Locate and identify every blood parasite.
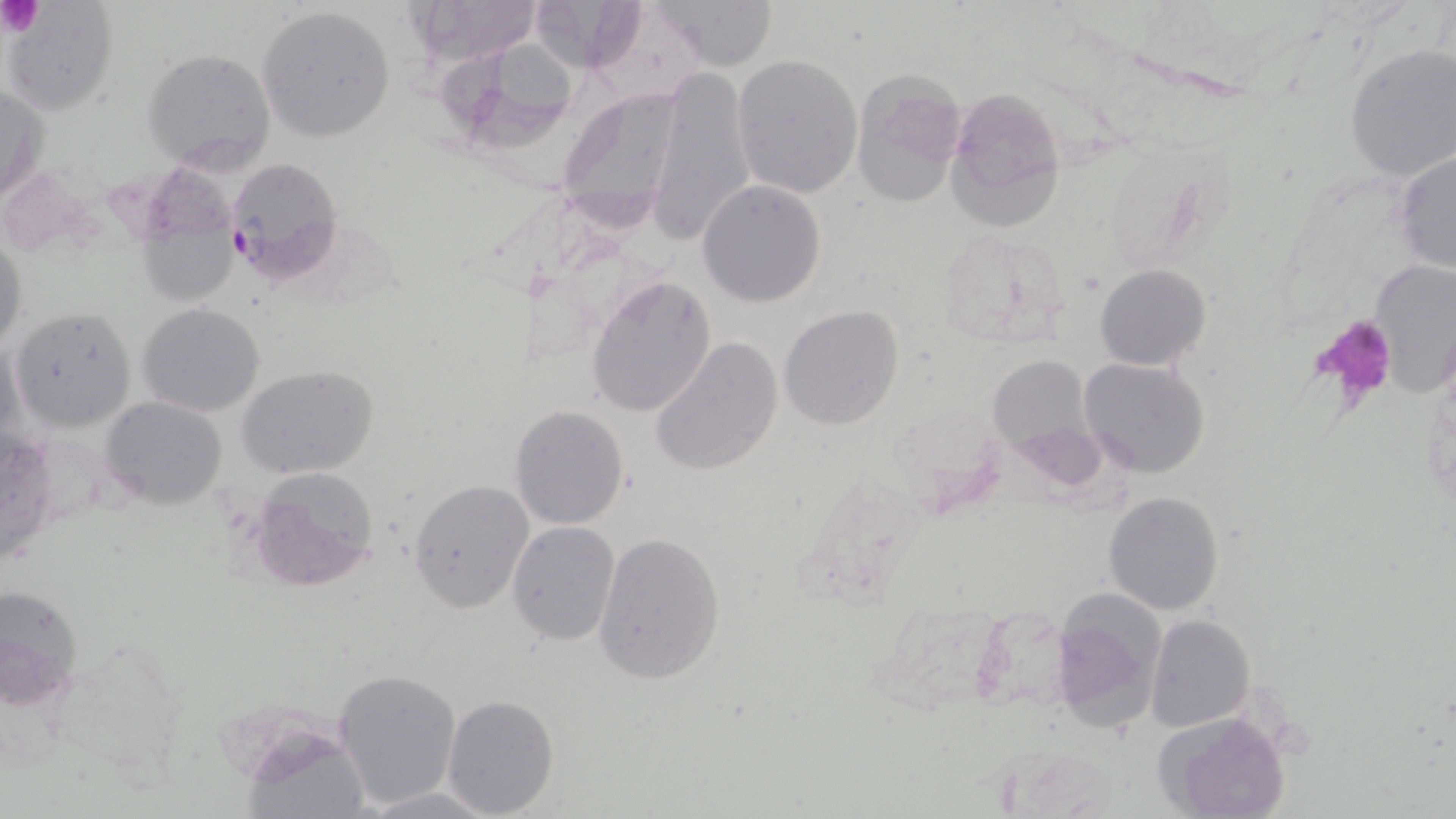

Approximate bounding boxes as (x1, y1, x2, y2) in pixels.
Plasmodium falciparum-infected red blood cells: (223, 157, 341, 280).
No Plasmodium ovale, Plasmodium malariae, Plasmodium vivax, Babesia divergens, or Trypanosoma brucei observed.

Summary:
  - Uninfected red blood cell locations: (408, 0, 547, 65), (532, 0, 650, 82), (650, 0, 779, 70), (4, 2, 118, 114), (258, 7, 398, 144), (1343, 45, 1456, 181), (437, 48, 579, 150), (142, 49, 275, 170), (732, 54, 862, 199), (645, 68, 756, 246), (849, 70, 966, 209), (1, 82, 48, 206), (556, 86, 692, 232), (943, 89, 1066, 231), (133, 151, 252, 304), (1393, 151, 1456, 276), (697, 180, 827, 307), (932, 229, 1070, 346), (0, 232, 27, 355), (1369, 258, 1456, 395), (1095, 263, 1210, 370), (585, 274, 717, 418), (137, 303, 264, 417), (778, 305, 905, 432), (11, 308, 137, 432), (649, 338, 783, 477), (988, 353, 1093, 457), (1079, 358, 1210, 479), (239, 364, 378, 480), (102, 395, 225, 509), (509, 405, 630, 530), (246, 468, 382, 594), (407, 478, 534, 616), (1103, 490, 1225, 616), (506, 521, 621, 646), (592, 529, 728, 686), (0, 583, 85, 709), (1048, 590, 1167, 735), (1146, 614, 1254, 732), (332, 668, 462, 808), (442, 694, 560, 817), (1160, 710, 1292, 819), (247, 731, 375, 818), (986, 742, 1128, 815), (361, 786, 497, 818)
  - Platelet locations: (0, 0, 45, 36), (1310, 315, 1398, 405)
  - Slide-level diagnosis: Plasmodium falciparum
  - Image size: 1456×819 pixels
  - Stain: May-Grünwald-Giemsa
  - Magnification: 1000x
  - Field of view: one of a larger specimen
  - Preparation: thin blood film
  - Modality: optical microscopy